Locate and identify every blood parasite.
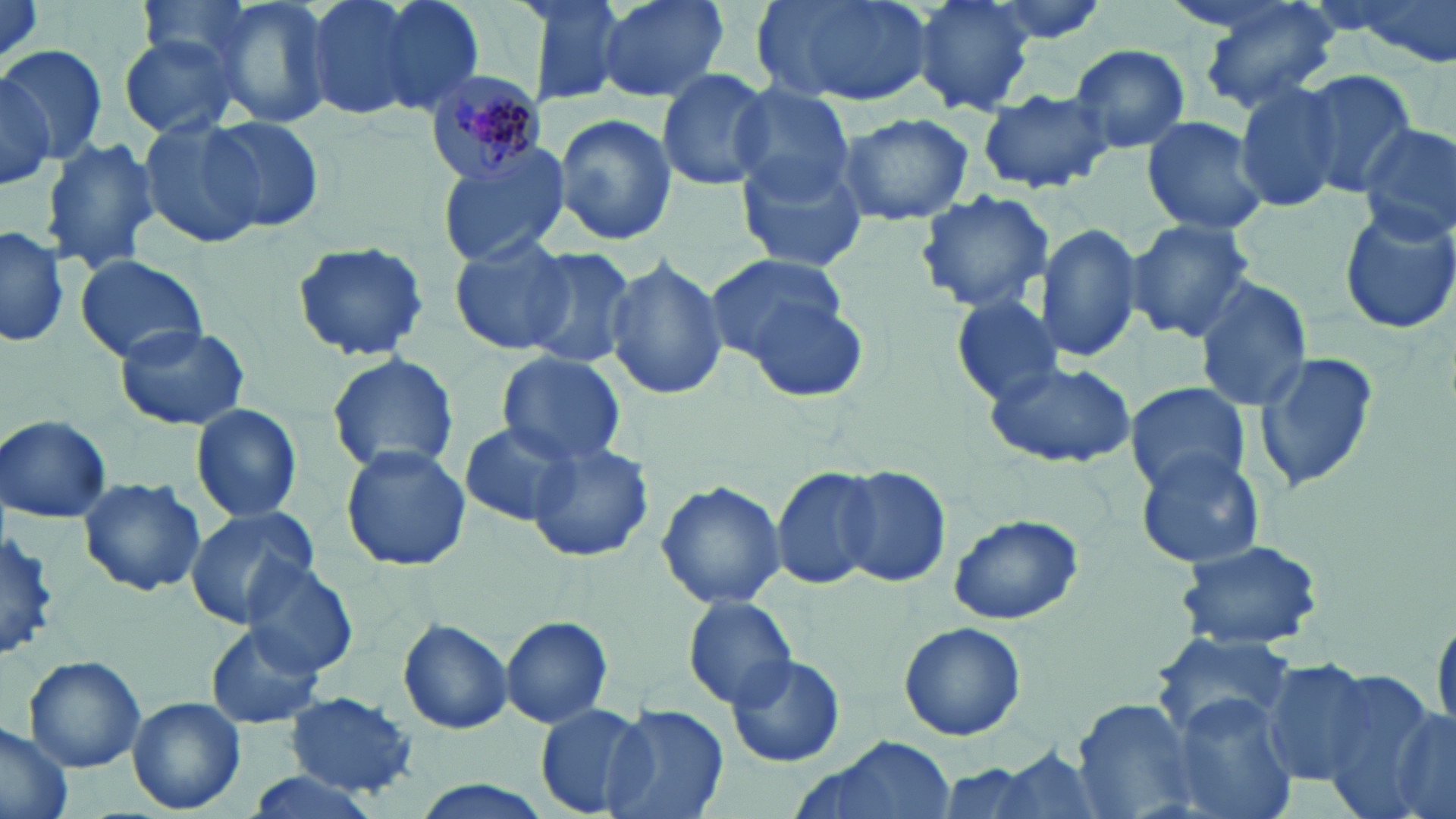
Approximate bounding boxes as (x1, y1, x2, y2) in pixels.
Plasmodium malariae-infected red blood cells: (424, 68, 547, 183).
No Plasmodium falciparum, Plasmodium ovale, Plasmodium vivax, Babesia divergens, or Trypanosoma brucei observed.

Summary:
  - Uninfected red blood cell locations: (134, 0, 266, 78), (207, 0, 335, 133), (304, 0, 453, 123), (371, 0, 486, 118), (509, 0, 630, 110), (595, 0, 730, 104), (752, 0, 938, 110), (911, 0, 1035, 117), (972, 0, 1113, 47), (1195, 0, 1342, 116), (1352, 0, 1456, 67), (117, 35, 243, 139), (1068, 42, 1192, 153), (1, 43, 106, 164), (0, 66, 55, 196), (655, 67, 776, 193), (1299, 69, 1420, 195), (729, 82, 855, 203), (1235, 83, 1347, 213), (978, 86, 1114, 194), (835, 110, 975, 226), (553, 112, 676, 247), (138, 114, 267, 249), (203, 115, 325, 232), (1140, 115, 1270, 239), (1355, 120, 1456, 243), (39, 137, 159, 276), (435, 143, 574, 267), (735, 148, 872, 273), (914, 188, 1055, 316), (1335, 201, 1456, 337), (1125, 219, 1256, 344), (1035, 221, 1144, 364), (1, 224, 69, 351), (450, 233, 575, 357), (290, 241, 431, 363), (518, 245, 638, 368), (74, 253, 209, 367), (603, 254, 727, 403), (706, 254, 853, 369), (1192, 278, 1312, 411), (734, 281, 873, 403), (951, 295, 1063, 405), (115, 324, 251, 430), (1255, 349, 1380, 492), (325, 351, 461, 476), (497, 355, 628, 464), (984, 360, 1136, 469), (1125, 381, 1249, 496), (190, 402, 303, 524), (1, 415, 112, 523), (461, 421, 584, 526), (526, 441, 654, 563), (338, 445, 472, 572), (1134, 449, 1266, 570), (769, 463, 883, 590), (834, 464, 952, 588), (78, 475, 206, 597), (656, 477, 787, 611), (182, 504, 320, 628), (947, 511, 1084, 626), (0, 527, 63, 662), (1175, 537, 1326, 652), (239, 558, 359, 677), (683, 592, 801, 709), (1430, 604, 1456, 743), (500, 614, 614, 729), (397, 617, 514, 735), (898, 621, 1026, 742), (206, 624, 324, 730), (1153, 634, 1298, 741), (163, 647, 279, 768), (723, 651, 844, 768), (22, 655, 146, 772), (1263, 660, 1379, 784), (1313, 670, 1451, 814), (284, 692, 421, 797), (1168, 693, 1296, 819), (127, 697, 246, 815), (1073, 697, 1204, 819), (1382, 701, 1456, 819), (535, 702, 654, 818), (600, 702, 729, 819), (0, 722, 76, 819), (790, 736, 960, 819), (991, 745, 1108, 819), (932, 762, 1057, 819), (238, 769, 385, 819), (409, 779, 557, 819)
  - Slide-level diagnosis: Plasmodium malariae
  - Magnification: 1000x
  - Field of view: single
  - Stain: May-Grünwald-Giemsa
  - Modality: optical microscopy
  - Image size: 1456×819 pixels
  - Preparation: thin blood film